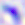
magnification: 400x
identification: Toxoplasma gondii
modality: micrograph